Locate every uninfected red blood cell.
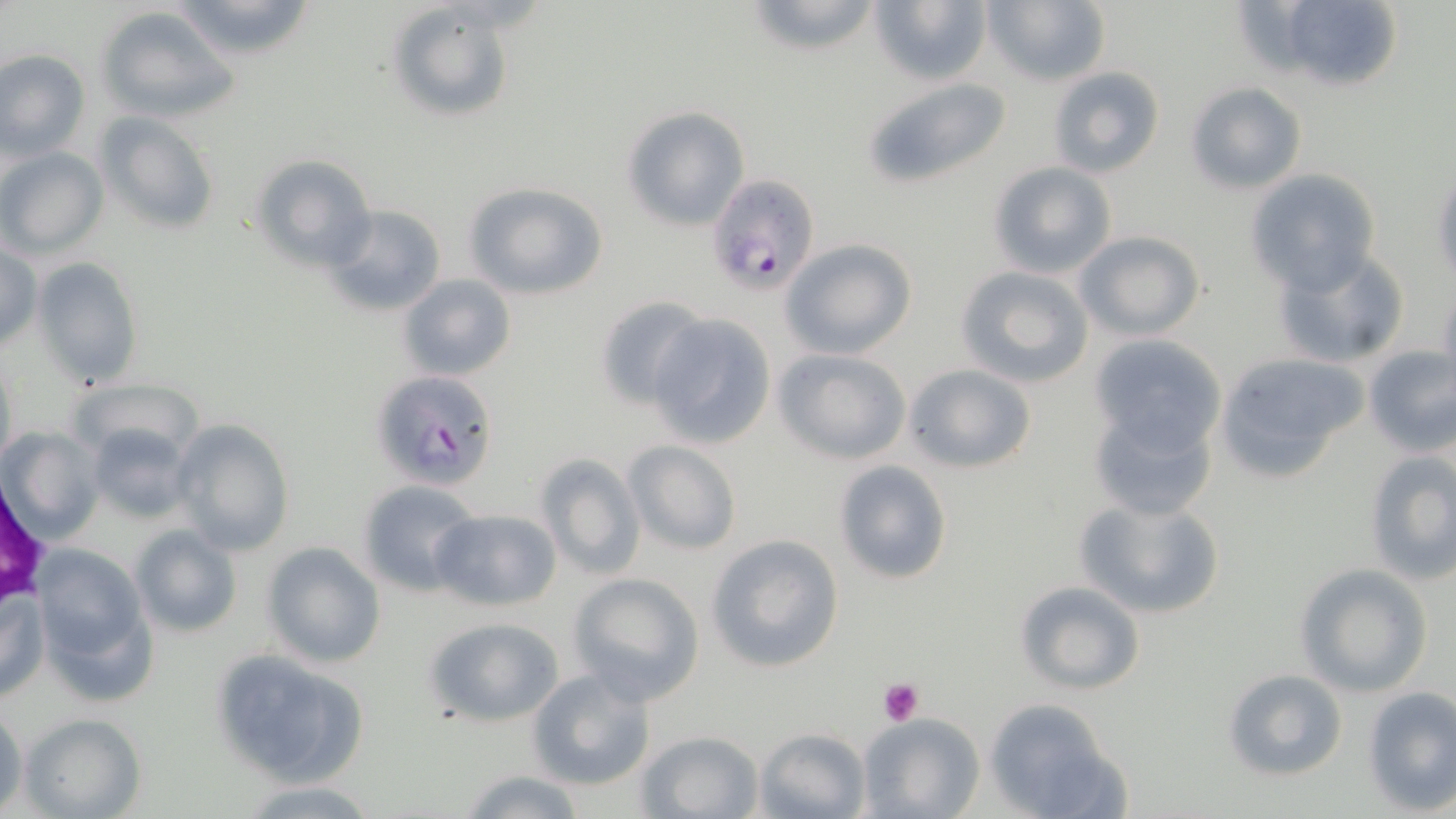
Approximate bounding boxes as (x1,y1)-(x2,y2) corner pairs in pixels.
Uninfected red blood cells: (168,0)-(321,64), (868,0)-(992,87), (981,0)-(1110,86), (1261,0)-(1407,93), (740,1)-(888,56), (385,4)-(515,124), (97,7)-(241,124), (0,49)-(90,162), (1048,66)-(1165,178), (861,76)-(1014,191), (1186,83)-(1306,194), (620,105)-(751,232), (95,109)-(221,234), (0,146)-(108,259), (251,155)-(377,271), (988,162)-(1117,280), (1245,169)-(1381,292), (1432,172)-(1455,283), (461,180)-(608,300), (320,203)-(448,317), (1076,232)-(1205,340), (780,238)-(919,359), (0,242)-(42,351), (1271,244)-(1412,368), (33,257)-(144,388), (956,265)-(1095,388), (398,273)-(517,382), (1437,282)-(1456,386), (593,294)-(710,410), (647,313)-(778,449), (1089,333)-(1226,453), (1361,343)-(1456,457), (772,347)-(912,465), (1215,352)-(1369,480), (1,355)-(18,475), (904,363)-(1037,473), (64,378)-(202,470), (1087,403)-(1219,520), (172,418)-(295,556), (84,422)-(195,522), (4,427)-(103,544), (623,440)-(741,554), (1363,451)-(1456,586), (534,452)-(645,580), (833,459)-(954,585), (357,480)-(482,596), (1071,493)-(1227,619), (429,508)-(561,611), (130,524)-(243,639), (706,534)-(845,674), (261,542)-(386,668), (33,545)-(150,686), (1296,563)-(1433,697), (569,572)-(705,704), (1015,580)-(1144,694), (1,586)-(46,706), (425,617)-(565,726), (209,648)-(371,785), (1223,667)-(1349,782), (527,668)-(656,791), (1362,686)-(1456,814), (982,699)-(1129,819), (0,704)-(26,814), (19,711)-(145,818), (857,712)-(984,818), (753,727)-(872,819), (636,729)-(763,818), (455,769)-(586,819), (243,780)-(381,817).

Platelet locations: (880,678)-(924,725). Plasmodium falciparum-infected red blood cell locations: (704,174)-(821,297), (368,370)-(501,492). Slide-level diagnosis: Plasmodium falciparum. May-Grünwald-Giemsa stain. Optical microscopy. Captured at 1000x magnification. Thin blood film. Image is 1456×819 pixels. One field of a larger specimen.